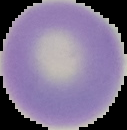

Malaria status: uninfected. From a thin blood film. Segmented cell region on a black background. Image is 127×130 pixels.